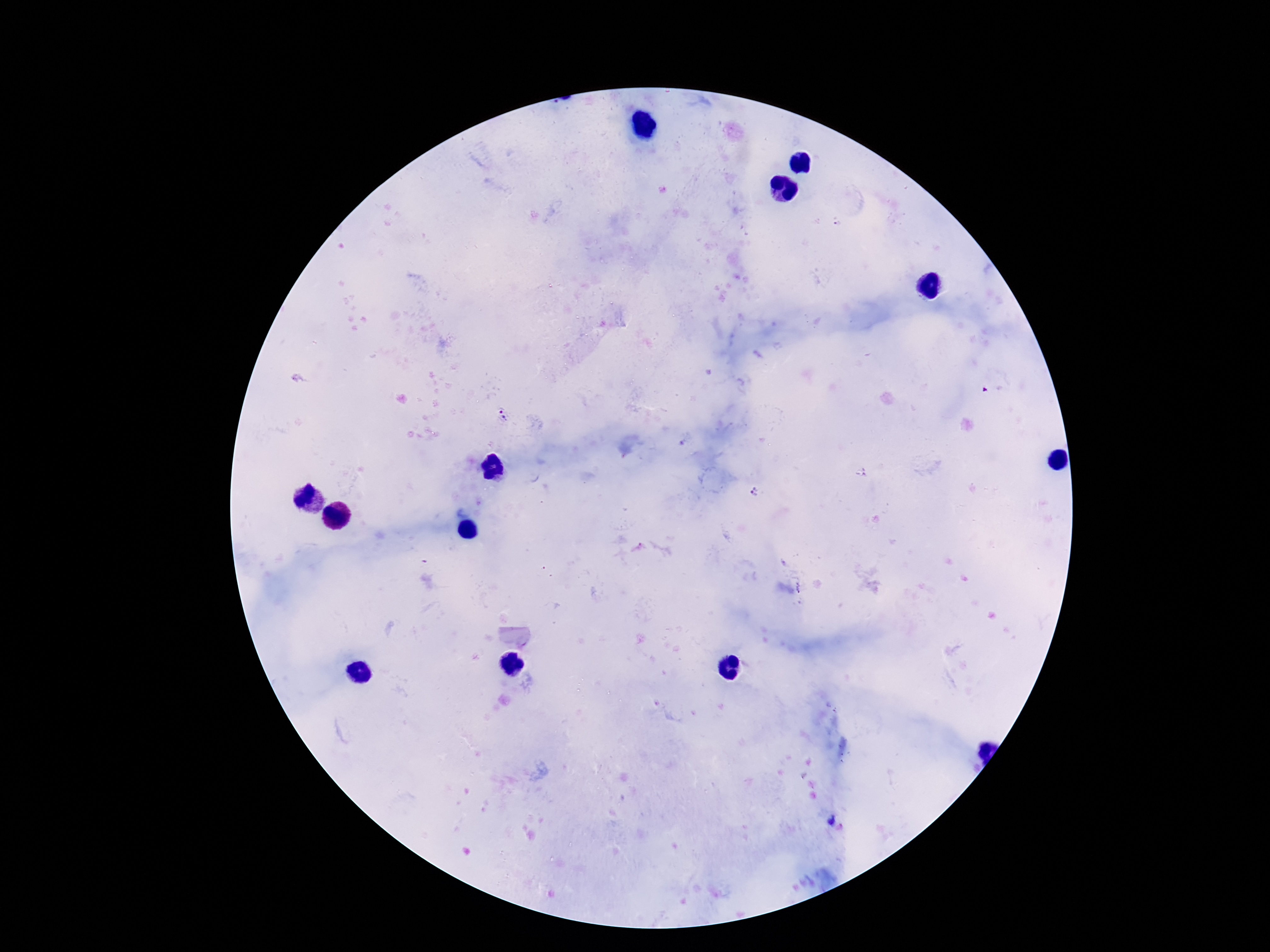

{
  "magnification": "100x",
  "stain": "Giemsa",
  "image_size": "1270×952 pixels",
  "field_of_view": "one from this slide",
  "plasmodium_parasite_locations": "approximate centers as {x, y} in pixels: {502, 416}, {757, 493}",
  "preparation": "thick blood film",
  "capture": "smartphone camera through the microscope eyepiece",
  "patient_malaria_status": "infected"
}